Outline platelets.
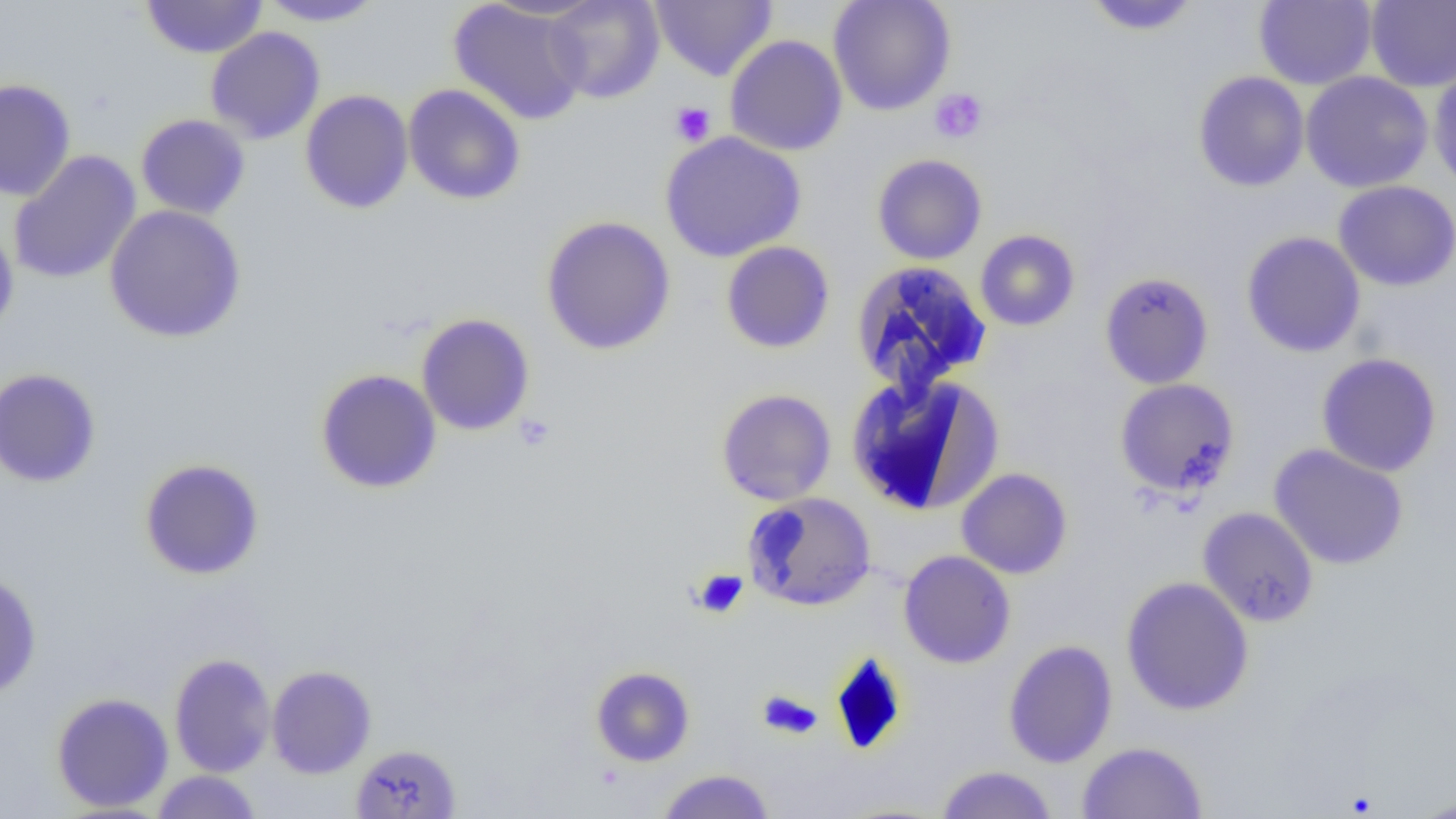
Approximate bounding boxes as (x1, y1, x2, y2) in pixels.
Platelets: (929, 88, 988, 144), (669, 101, 716, 146), (514, 413, 555, 450), (693, 569, 748, 618), (757, 691, 823, 739).

slide_level_diagnosis: negative for blood parasites
modality: light microscopy
image_size: 1456×819 pixels
magnification: 1000x
field_of_view: single
uninfected_red_blood_cell_locations: 'approximate bounding boxes as (x1, y1, x2, y2) in pixels: (140, 0, 268, 59), (255, 0, 388, 27), (448, 0, 590, 126), (544, 0, 665, 104), (651, 0, 776, 82), (828, 0, 956, 116), (1082, 0, 1202, 36), (1253, 0, 1377, 90), (1366, 0, 1456, 92), (205, 27, 326, 145), (724, 34, 848, 157), (1429, 63, 1456, 193), (1193, 71, 1310, 192), (1300, 71, 1433, 193), (0, 78, 76, 202), (403, 84, 526, 205), (300, 89, 414, 214), (136, 113, 251, 219), (659, 131, 807, 263), (8, 150, 142, 284), (872, 153, 988, 265), (1333, 180, 1456, 291), (104, 205, 246, 343), (540, 215, 676, 356), (0, 222, 19, 338), (975, 229, 1080, 331), (1241, 231, 1366, 357), (721, 241, 836, 353), (849, 260, 992, 396), (1099, 271, 1214, 389), (416, 313, 535, 436), (1316, 352, 1442, 477), (0, 368, 102, 488), (315, 369, 442, 494), (845, 372, 1004, 517), (1114, 378, 1239, 499), (716, 388, 837, 505), (1268, 444, 1409, 570), (139, 458, 264, 580), (956, 468, 1073, 579), (742, 492, 876, 611), (1197, 506, 1319, 627), (898, 550, 1016, 668), (0, 571, 42, 699), (1121, 576, 1254, 716), (1003, 640, 1118, 769), (169, 653, 276, 777), (266, 665, 377, 779), (590, 666, 695, 766), (50, 692, 174, 813), (1076, 741, 1208, 818), (351, 744, 462, 818), (935, 765, 1058, 818), (655, 769, 776, 819), (151, 770, 263, 818), (1409, 793, 1456, 818)'
preparation: thin blood film